Assess this cell for malaria.
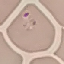

It is parasitized.

Giemsa stain. Photographed with a smartphone camera at the microscope eyepiece. Cell patch, automatically extracted from a larger field of view and resized to 64 × 64 pixels. Thin blood film.